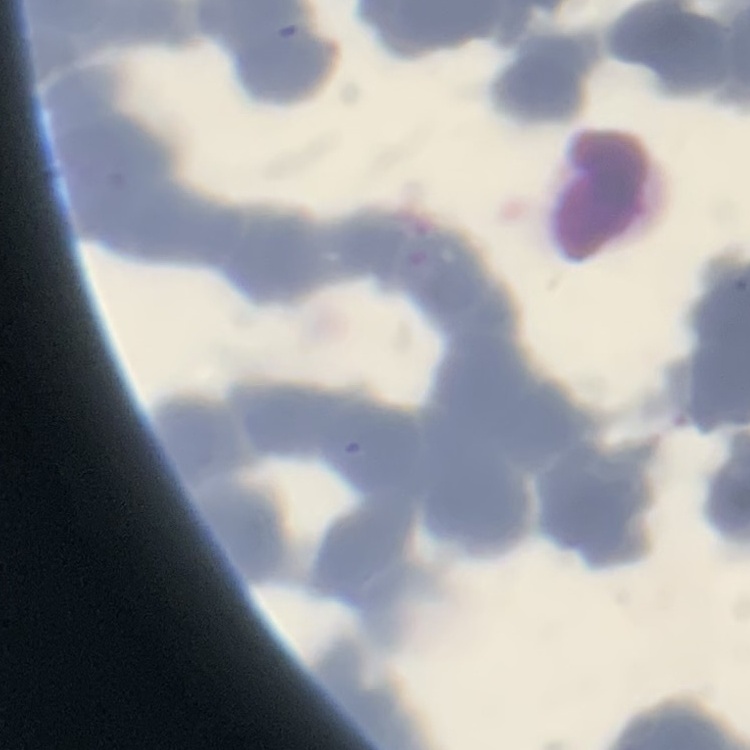

The erythrocytes exhibit rouleaux formation. Thin blood smear. Square crop of a larger photomicrograph. Stained with either Field's or Giemsa.